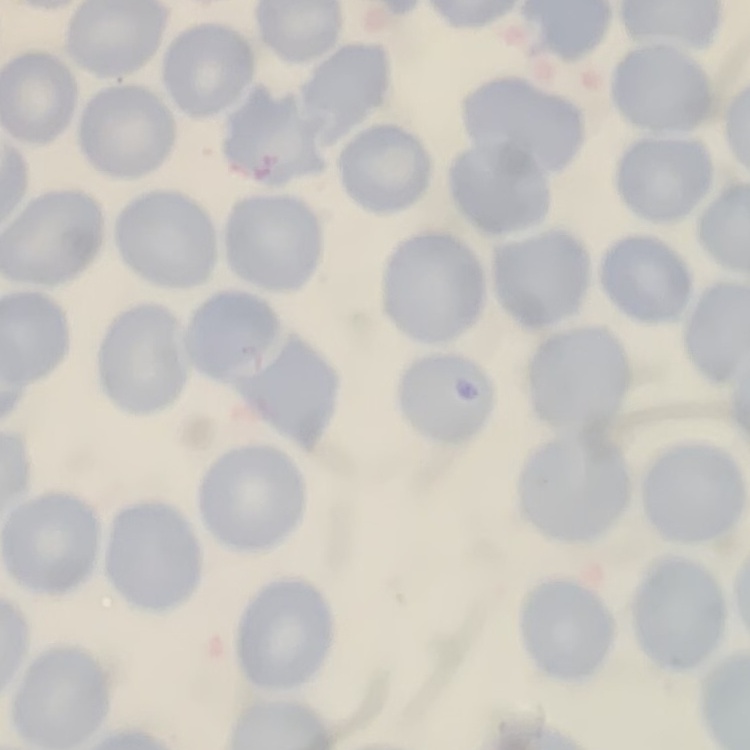
The erythrocytes show no rouleaux formation. Stained with either Field's or Giemsa. Thin peripheral smear. One tile cut from a larger photomicrograph.